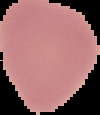

From a thin blood smear. Image is 100×115 pixels. Malaria status: uninfected. Segmented cell region on a black background.